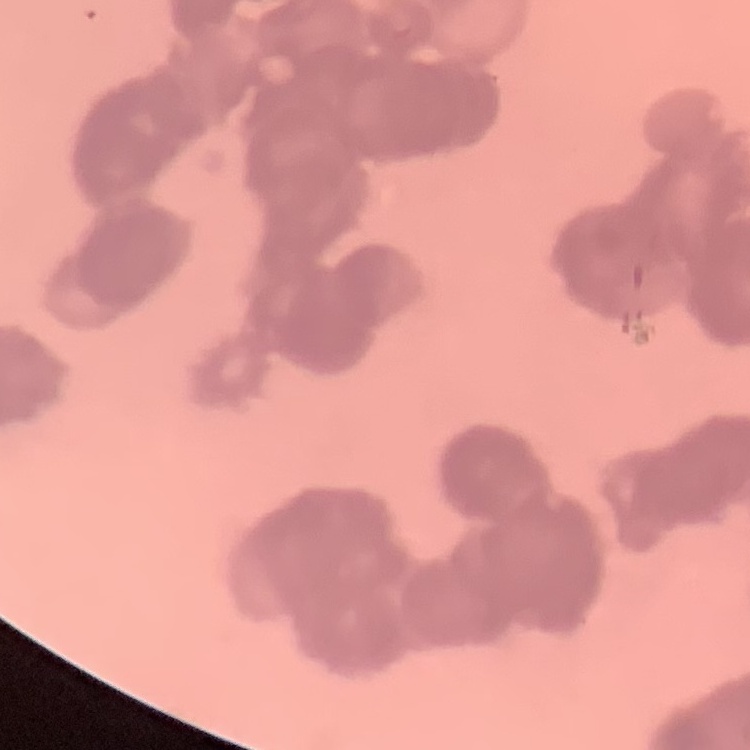
The red blood cells exhibit rouleaux formation. One tile cut from a larger photomicrograph. Thin blood film. Stained with either Field's or Giemsa.